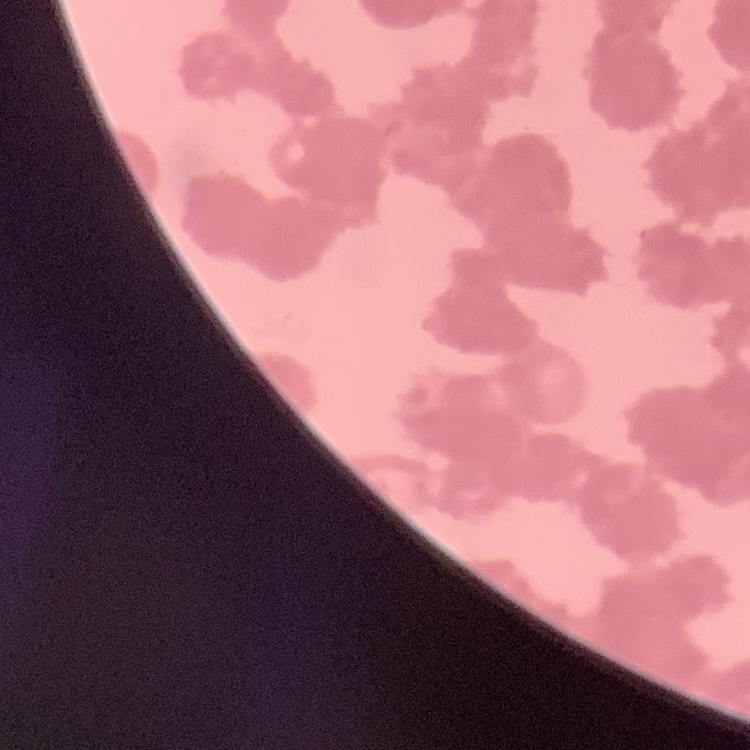

The red blood cells exhibit rouleaux formation. Stained with either Field's or Giemsa. One tile cut from a larger photomicrograph. Thin blood film.